Assess this cell for malaria.
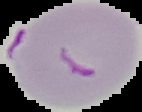
It is parasitized.

Image is 142×112 pixels. From a thin blood smear. The area outside the segmented cell region is set to black.